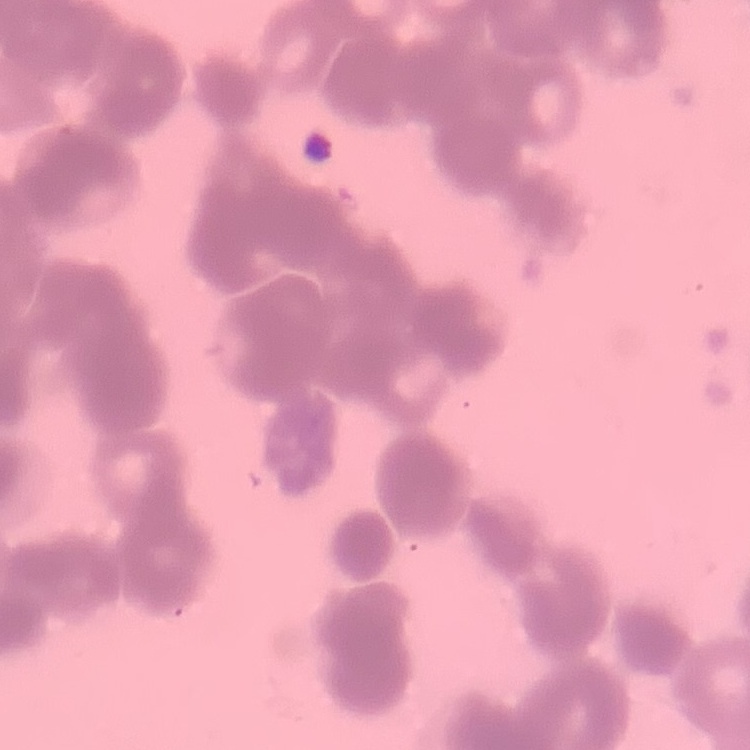

Summary:
  - Red blood cell morphology: rouleaux formation
  - Image type: one tile cut from a larger photomicrograph
  - Preparation: thin blood smear
  - Stain: Field's or Giemsa